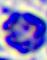

identification = white blood cell
modality = micrograph
magnification = 400x